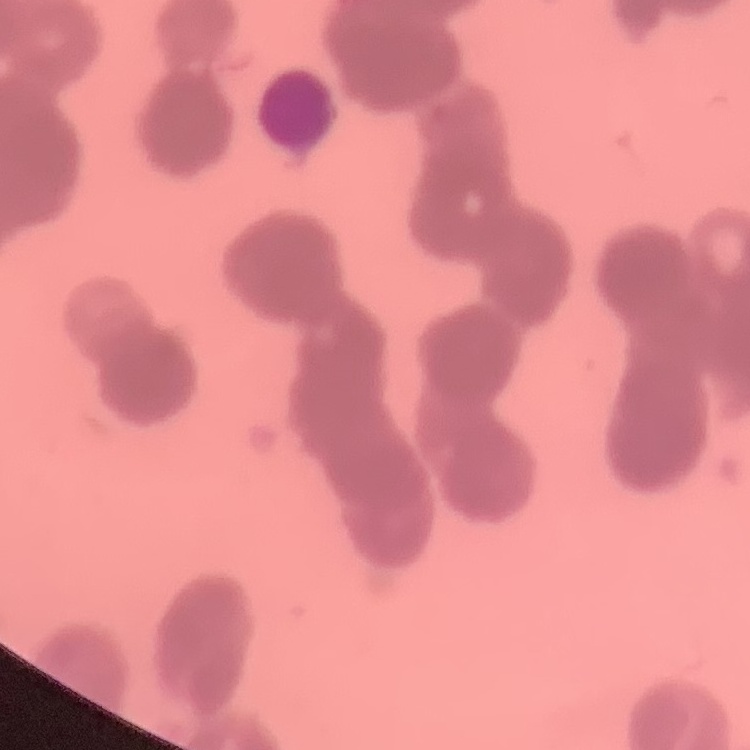

erythrocyte morphology = rouleaux formation
stain = Field's or Giemsa
image type = one tile cut from a larger photomicrograph
preparation = thin blood film